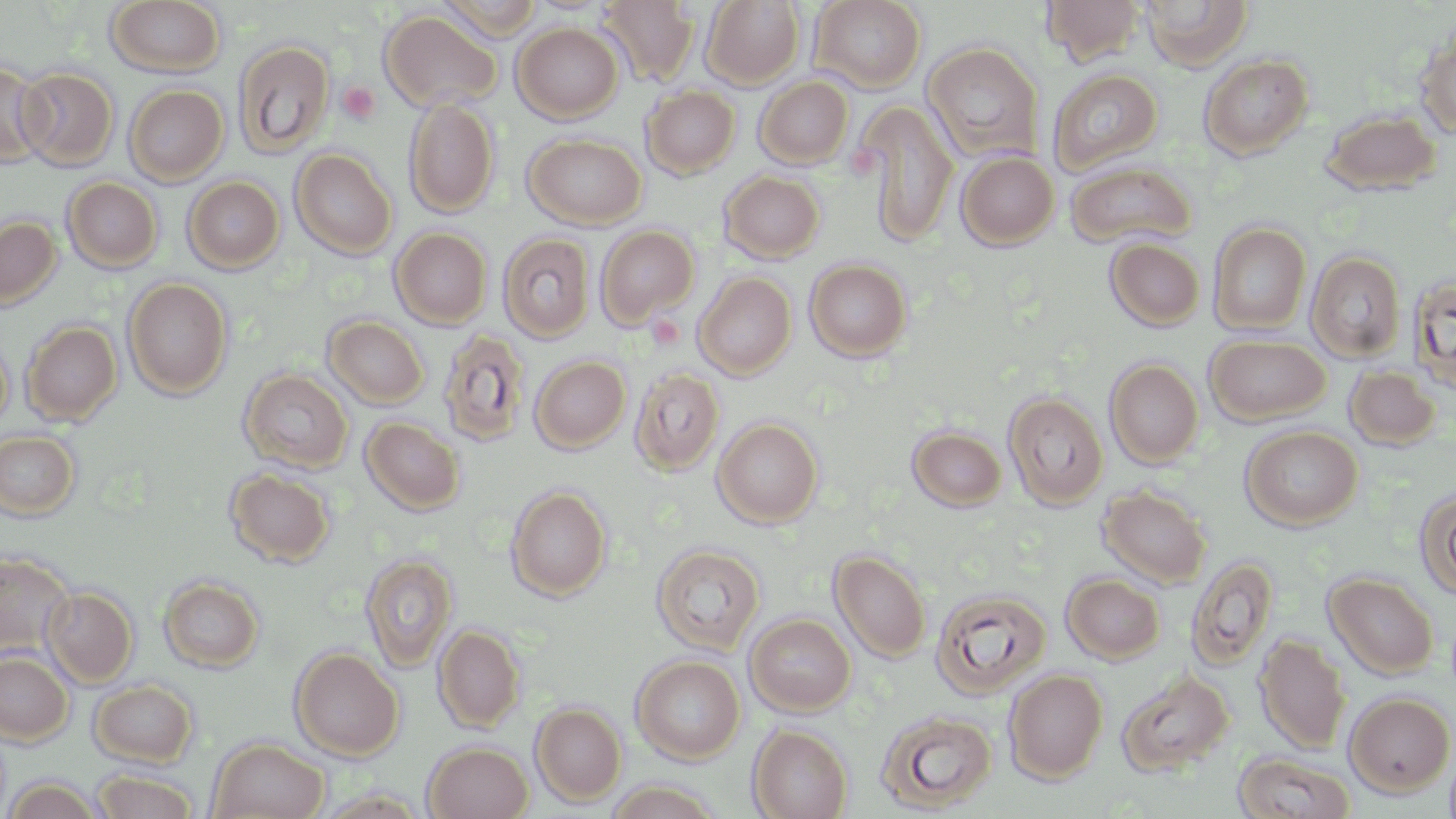 Approximate bounding boxes as named x1/y1/x2/y2 corners in pixels. Platelet locations: (x1=337, y1=80, x2=381, y2=124). Uninfected red blood cell locations: (x1=597, y1=0, x2=699, y2=85), (x1=702, y1=0, x2=804, y2=89), (x1=810, y1=0, x2=927, y2=93), (x1=1042, y1=0, x2=1146, y2=65), (x1=1141, y1=0, x2=1253, y2=69), (x1=106, y1=1, x2=226, y2=77), (x1=380, y1=9, x2=502, y2=112), (x1=512, y1=22, x2=623, y2=123), (x1=1415, y1=29, x2=1456, y2=138), (x1=233, y1=40, x2=334, y2=158), (x1=922, y1=41, x2=1043, y2=162), (x1=1199, y1=54, x2=1313, y2=159), (x1=0, y1=60, x2=51, y2=168), (x1=15, y1=67, x2=119, y2=171), (x1=1048, y1=68, x2=1163, y2=173), (x1=755, y1=76, x2=854, y2=169), (x1=124, y1=84, x2=229, y2=185), (x1=641, y1=85, x2=740, y2=179), (x1=404, y1=97, x2=500, y2=218), (x1=857, y1=100, x2=959, y2=247), (x1=1320, y1=109, x2=1442, y2=196), (x1=523, y1=132, x2=647, y2=229), (x1=290, y1=148, x2=397, y2=260), (x1=955, y1=150, x2=1059, y2=250), (x1=1065, y1=161, x2=1196, y2=249), (x1=719, y1=171, x2=825, y2=263), (x1=183, y1=176, x2=285, y2=273), (x1=63, y1=177, x2=162, y2=272), (x1=62, y1=178, x2=283, y2=270), (x1=0, y1=215, x2=62, y2=310), (x1=1208, y1=222, x2=1311, y2=335), (x1=595, y1=224, x2=699, y2=327), (x1=390, y1=227, x2=492, y2=328), (x1=498, y1=233, x2=595, y2=342), (x1=1105, y1=237, x2=1205, y2=331), (x1=1306, y1=250, x2=1407, y2=362), (x1=805, y1=258, x2=912, y2=362), (x1=694, y1=272, x2=797, y2=379), (x1=1408, y1=274, x2=1456, y2=394), (x1=123, y1=278, x2=233, y2=398), (x1=323, y1=316, x2=429, y2=409), (x1=22, y1=321, x2=121, y2=426), (x1=438, y1=329, x2=531, y2=446), (x1=0, y1=334, x2=13, y2=434), (x1=1204, y1=334, x2=1331, y2=424), (x1=529, y1=355, x2=631, y2=453), (x1=1104, y1=358, x2=1204, y2=468), (x1=1345, y1=366, x2=1441, y2=451), (x1=630, y1=368, x2=725, y2=475), (x1=239, y1=369, x2=353, y2=472), (x1=1003, y1=391, x2=1109, y2=509), (x1=361, y1=417, x2=464, y2=515), (x1=712, y1=418, x2=823, y2=528), (x1=906, y1=425, x2=1007, y2=512), (x1=1240, y1=426, x2=1363, y2=530), (x1=0, y1=430, x2=81, y2=521), (x1=225, y1=468, x2=336, y2=567), (x1=1098, y1=484, x2=1212, y2=588), (x1=506, y1=485, x2=611, y2=601), (x1=1414, y1=487, x2=1456, y2=601), (x1=651, y1=544, x2=765, y2=655), (x1=830, y1=549, x2=931, y2=662), (x1=0, y1=552, x2=74, y2=659), (x1=360, y1=552, x2=457, y2=671), (x1=1186, y1=555, x2=1279, y2=670), (x1=1323, y1=572, x2=1439, y2=679), (x1=1062, y1=573, x2=1165, y2=664), (x1=159, y1=575, x2=264, y2=672), (x1=42, y1=586, x2=137, y2=686), (x1=930, y1=587, x2=1052, y2=699), (x1=745, y1=614, x2=855, y2=716), (x1=434, y1=623, x2=525, y2=734), (x1=1255, y1=634, x2=1350, y2=754), (x1=290, y1=647, x2=403, y2=760), (x1=0, y1=651, x2=73, y2=746), (x1=631, y1=655, x2=745, y2=763), (x1=1116, y1=668, x2=1235, y2=778), (x1=1003, y1=669, x2=1108, y2=783), (x1=90, y1=680, x2=198, y2=767), (x1=1344, y1=691, x2=1455, y2=796), (x1=530, y1=702, x2=627, y2=806), (x1=876, y1=709, x2=997, y2=813), (x1=749, y1=724, x2=853, y2=819), (x1=207, y1=737, x2=329, y2=818), (x1=422, y1=740, x2=533, y2=819), (x1=1444, y1=742, x2=1456, y2=819), (x1=1233, y1=751, x2=1356, y2=819), (x1=92, y1=769, x2=199, y2=818), (x1=4, y1=776, x2=105, y2=819), (x1=601, y1=778, x2=724, y2=819). Slide-level diagnosis: no evidence of blood parasites. Image is 1456×819 pixels. One field of a larger specimen. Optical microscopy. Thin blood film. May-Grünwald-Giemsa-stained preparation. 1000x magnification.